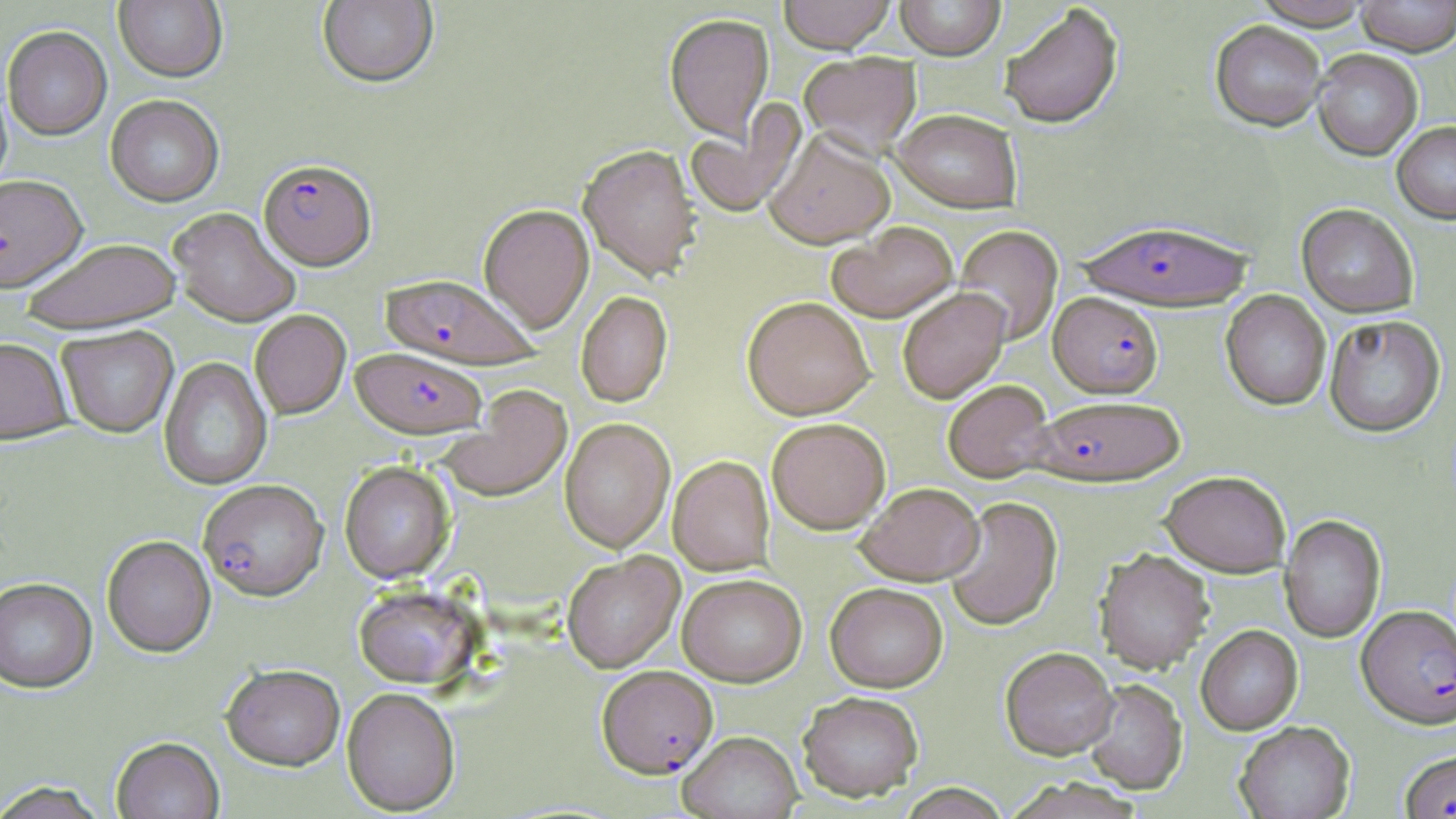

slide_level_diagnosis: Plasmodium falciparum
field_of_view: one of a larger specimen
plasmodium_falciparum_infected_red_blood_cell_locations: 'approximate bounding boxes as [x1, y1, x2, y2] in pixels: [259, 158, 376, 270], [1078, 218, 1254, 311], [382, 274, 539, 369], [1049, 292, 1163, 397], [351, 347, 486, 440], [1032, 395, 1184, 486], [198, 479, 329, 602], [1357, 604, 1456, 729], [597, 665, 718, 778], [1399, 749, 1456, 819]'
magnification: 1000x
uninfected_red_blood_cell_locations: 'approximate bounding boxes as [x1, y1, x2, y2] in pixels: [317, 0, 438, 89], [778, 0, 896, 53], [895, 0, 1004, 60], [1252, 0, 1373, 29], [1355, 0, 1456, 56], [114, 1, 226, 83], [999, 4, 1124, 129], [664, 14, 775, 143], [1210, 20, 1327, 131], [2, 27, 112, 141], [1312, 48, 1423, 160], [799, 53, 921, 156], [105, 95, 224, 207], [685, 102, 806, 220], [892, 108, 1022, 213], [1392, 122, 1456, 223], [765, 129, 894, 248], [573, 148, 702, 282], [0, 175, 87, 293], [479, 203, 594, 333], [1297, 204, 1419, 317], [168, 207, 300, 328], [828, 221, 958, 323], [953, 225, 1063, 345], [21, 238, 182, 333], [897, 288, 1011, 404], [1220, 290, 1331, 410], [576, 291, 672, 407], [742, 295, 875, 419], [249, 310, 351, 419], [1324, 314, 1445, 437], [58, 326, 178, 438], [0, 337, 73, 444], [159, 357, 272, 490], [942, 379, 1054, 482], [436, 384, 572, 503], [559, 418, 675, 553], [767, 418, 891, 534], [668, 456, 774, 575], [339, 461, 455, 584], [1160, 470, 1291, 576], [856, 482, 984, 585], [944, 495, 1063, 632], [1280, 514, 1386, 643], [102, 535, 216, 658], [1094, 548, 1214, 673], [562, 552, 684, 673], [677, 573, 807, 686], [0, 578, 97, 694], [825, 582, 948, 692], [354, 584, 482, 690], [1196, 625, 1302, 734], [1000, 646, 1118, 759], [221, 665, 345, 772], [1082, 679, 1188, 794], [341, 688, 460, 815], [798, 690, 924, 801], [1234, 721, 1355, 819], [678, 730, 802, 819], [112, 737, 224, 819], [1004, 777, 1148, 819], [0, 781, 110, 819], [892, 783, 1014, 818]'
image_size: 1456×819 pixels
preparation: thin blood smear
modality: light microscopy
stain: May-Grünwald-Giemsa